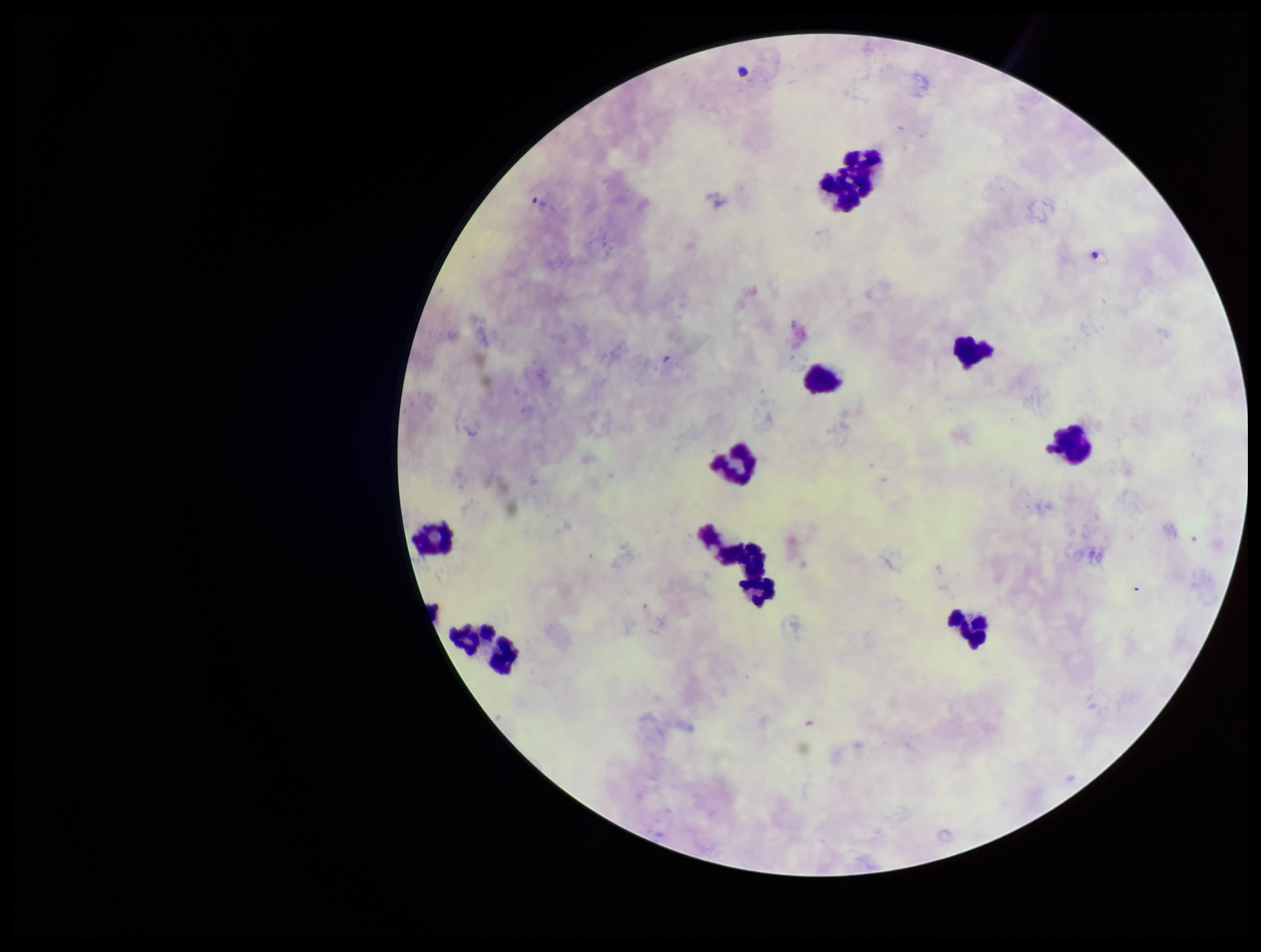

Photographed through the microscope eyepiece with a smartphone camera. Image is 1261×952 pixels. Patient malaria status: infected. Species reported for this patient: Plasmodium vivax. One field from this slide. Leukocyte count: 12. Parasite count: 0. Preparation: thick smear. Plasmodium parasites: none identified. Stained with Giemsa.